Outline each blood parasite and name the species.
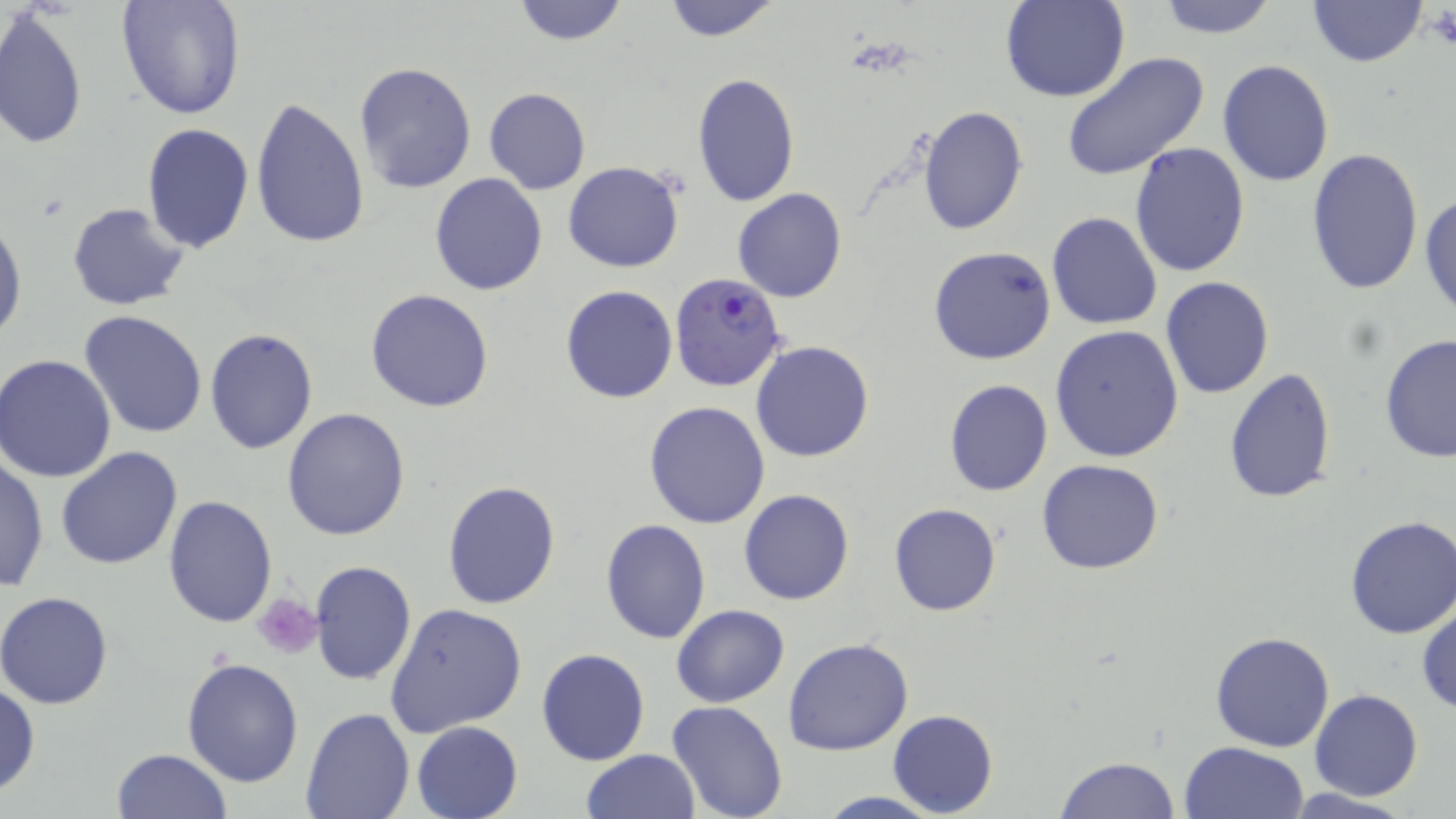
Approximate bounding boxes as (x1,y1)-(x2,y2) corner pairs in pixels.
Plasmodium falciparum-infected red blood cells: (671,272)-(786,392).
No Plasmodium ovale, Plasmodium malariae, Plasmodium vivax, Babesia divergens, or Trypanosoma brucei observed.

slide_level_diagnosis: Plasmodium falciparum
uninfected_red_blood_cell_locations: 'approximate bounding boxes as (x1,y1)-(x2,y2) corner pairs in pixels: (115,0)-(247,121), (660,0)-(783,42), (1002,0)-(1129,103), (1153,0)-(1280,39), (1307,0)-(1426,68), (509,1)-(632,47), (0,7)-(88,153), (1061,53)-(1210,182), (1218,59)-(1334,187), (353,61)-(476,195), (691,72)-(801,210), (483,87)-(591,195), (249,97)-(371,250), (917,105)-(1028,234), (141,125)-(254,253), (1130,143)-(1252,278), (1306,146)-(1425,296), (563,162)-(685,272), (429,173)-(547,294), (732,187)-(847,304), (1419,190)-(1456,321), (67,202)-(192,311), (1046,211)-(1163,329), (0,215)-(25,342), (929,246)-(1057,365), (1160,276)-(1274,398), (560,284)-(677,403), (366,288)-(495,412), (78,309)-(209,438), (1050,326)-(1184,465), (204,328)-(319,455), (1379,334)-(1456,463), (751,341)-(875,462), (2,354)-(119,482), (1223,366)-(1338,504), (942,379)-(1053,496), (644,401)-(770,529), (282,407)-(411,542), (55,447)-(183,570), (1,456)-(48,594), (1036,458)-(1165,574), (442,480)-(560,609), (739,489)-(853,605), (165,494)-(277,628), (889,503)-(1001,617), (1342,515)-(1456,641), (602,518)-(711,645), (308,560)-(416,686), (1,592)-(117,708), (1417,600)-(1455,714), (384,603)-(527,739), (670,604)-(790,708), (1208,631)-(1335,753), (783,637)-(913,755), (536,647)-(650,766), (181,658)-(305,788), (0,682)-(40,797), (1309,689)-(1423,801), (667,700)-(787,819), (299,705)-(415,819), (888,709)-(997,817), (412,720)-(524,819), (1178,740)-(1310,819), (111,748)-(233,818), (580,749)-(701,819), (1054,757)-(1183,818), (1281,789)-(1419,818), (813,791)-(949,819)'
field_of_view: single
preparation: thin blood smear
magnification: 1000x
image_size: 1456×819 pixels
platelet_locations: 'approximate bounding boxes as (x1,y1)-(x2,y2) corner pairs in pixels: (1427,6)-(1456,52), (255,593)-(321,659)'
modality: light microscopy
stain: May-Grünwald-Giemsa